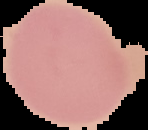

Summary:
  - Image size: 148×130 pixels
  - Malaria status: uninfected
  - Preparation: thin blood smear
  - Image type: cell region segmented out of the field of view; surrounding area masked to black